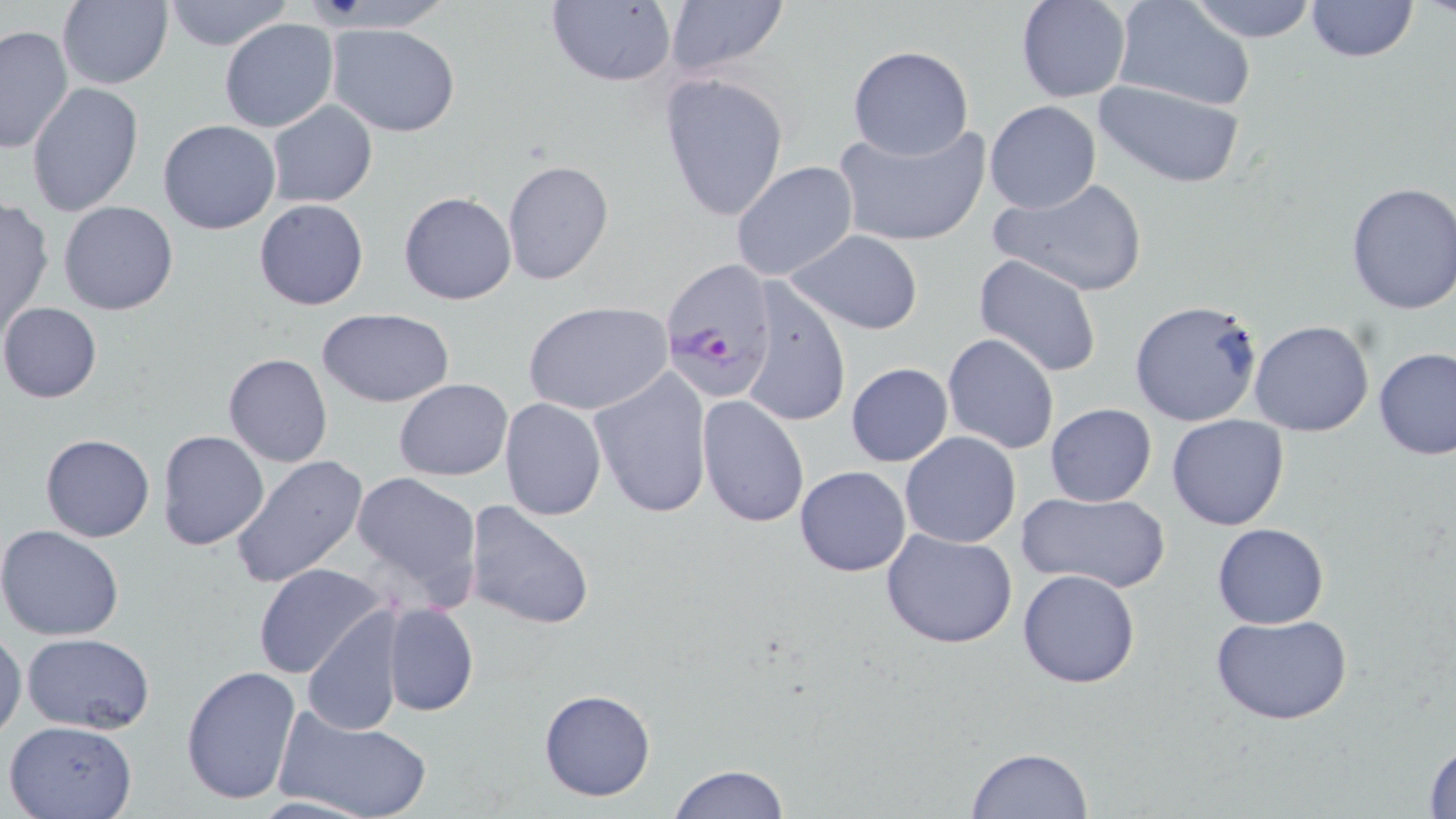

Summary:
  - Coordinate format: approximate bounding boxes as named x1/y1/x2/y2 corners in pixels
  - Uninfected red blood cell locations: (x1=58, y1=0, x2=174, y2=91), (x1=161, y1=0, x2=293, y2=52), (x1=547, y1=0, x2=675, y2=87), (x1=1185, y1=0, x2=1321, y2=42), (x1=1302, y1=0, x2=1421, y2=63), (x1=661, y1=1, x2=790, y2=81), (x1=1014, y1=1, x2=1131, y2=102), (x1=1108, y1=5, x2=1254, y2=112), (x1=219, y1=18, x2=339, y2=133), (x1=328, y1=22, x2=460, y2=135), (x1=1, y1=24, x2=75, y2=155), (x1=847, y1=45, x2=973, y2=160), (x1=659, y1=72, x2=790, y2=223), (x1=1092, y1=78, x2=1247, y2=191), (x1=26, y1=82, x2=143, y2=217), (x1=985, y1=100, x2=1101, y2=213), (x1=266, y1=101, x2=378, y2=208), (x1=158, y1=119, x2=282, y2=235), (x1=833, y1=120, x2=992, y2=248), (x1=502, y1=160, x2=613, y2=285), (x1=730, y1=161, x2=858, y2=283), (x1=989, y1=176, x2=1147, y2=299), (x1=1344, y1=180, x2=1456, y2=315), (x1=398, y1=191, x2=517, y2=306), (x1=254, y1=199, x2=370, y2=311), (x1=0, y1=200, x2=53, y2=336), (x1=59, y1=201, x2=178, y2=315), (x1=786, y1=229, x2=924, y2=335), (x1=973, y1=254, x2=1103, y2=379), (x1=738, y1=281, x2=852, y2=429), (x1=522, y1=300, x2=673, y2=416), (x1=1129, y1=300, x2=1264, y2=427), (x1=0, y1=302, x2=103, y2=404), (x1=316, y1=309, x2=454, y2=407), (x1=1248, y1=319, x2=1375, y2=437), (x1=942, y1=333, x2=1060, y2=455), (x1=1373, y1=347, x2=1455, y2=460), (x1=223, y1=353, x2=333, y2=468), (x1=845, y1=362, x2=953, y2=467), (x1=588, y1=366, x2=711, y2=519), (x1=395, y1=378, x2=513, y2=481), (x1=697, y1=395, x2=810, y2=526), (x1=499, y1=398, x2=606, y2=520), (x1=1045, y1=402, x2=1157, y2=507), (x1=1166, y1=413, x2=1290, y2=531), (x1=157, y1=429, x2=270, y2=551), (x1=900, y1=431, x2=1021, y2=547), (x1=40, y1=432, x2=154, y2=543), (x1=230, y1=455, x2=369, y2=588), (x1=795, y1=465, x2=911, y2=576), (x1=351, y1=471, x2=481, y2=605), (x1=1016, y1=490, x2=1172, y2=594), (x1=463, y1=499, x2=598, y2=633), (x1=1212, y1=523, x2=1329, y2=628), (x1=0, y1=524, x2=125, y2=641), (x1=881, y1=528, x2=1018, y2=649), (x1=253, y1=563, x2=387, y2=680), (x1=1018, y1=568, x2=1140, y2=688), (x1=382, y1=602, x2=478, y2=716), (x1=301, y1=611, x2=405, y2=738), (x1=1209, y1=613, x2=1358, y2=727), (x1=0, y1=630, x2=25, y2=739), (x1=23, y1=633, x2=155, y2=734), (x1=180, y1=664, x2=302, y2=806), (x1=538, y1=688, x2=655, y2=802), (x1=275, y1=708, x2=432, y2=819), (x1=4, y1=718, x2=138, y2=819), (x1=1423, y1=737, x2=1456, y2=819), (x1=966, y1=745, x2=1094, y2=818), (x1=666, y1=763, x2=791, y2=819)
  - Plasmodium falciparum-infected red blood cell locations: (x1=662, y1=259, x2=780, y2=399)
  - Slide-level diagnosis: Plasmodium falciparum
  - Field of view: one of a larger specimen
  - Stain: May-Grünwald-Giemsa
  - Preparation: thin blood smear
  - Image size: 1456×819 pixels
  - Magnification: 1000x
  - Modality: light microscopy